Give the extent of all Trypanosoma brucei.
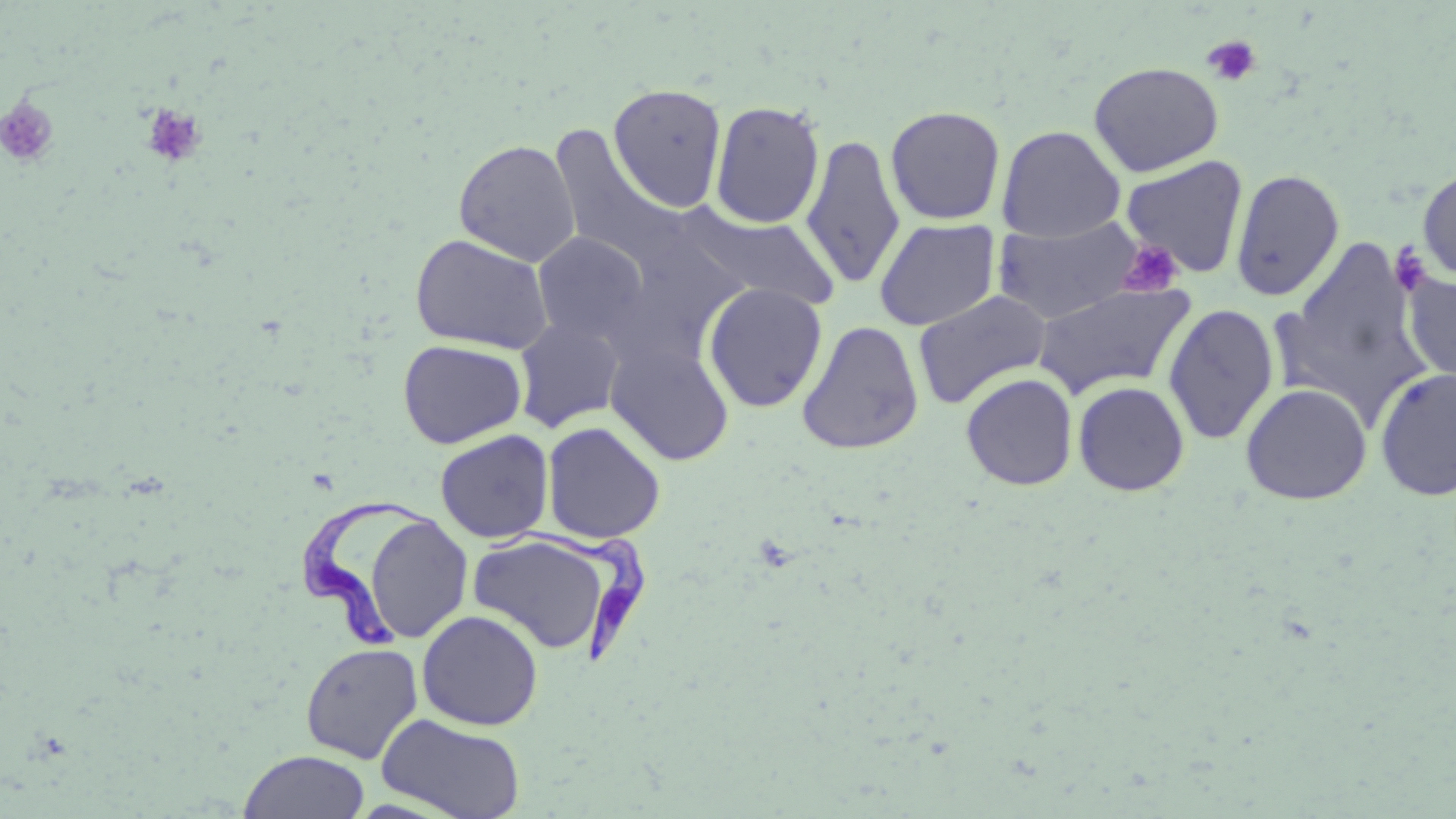

Approximate bounding boxes as named x1/y1/x2/y2 corners in pixels.
Trypanosoma brucei: (x1=299, y1=496, x2=452, y2=650), (x1=484, y1=519, x2=649, y2=666).

slide_level_diagnosis: Trypanosoma brucei
modality: optical microscopy
image_size: 1456×819 pixels
preparation: thin blood smear
field_of_view: single
platelet_locations: 'approximate bounding boxes as named x1/y1/x2/y2 corners in pixels: (x1=1202, y1=36, x2=1261, y2=87), (x1=0, y1=96, x2=60, y2=168), (x1=141, y1=104, x2=208, y2=168), (x1=1116, y1=239, x2=1183, y2=297), (x1=1387, y1=242, x2=1434, y2=298)'
stain: May-Grünwald-Giemsa
uninfected_red_blood_cell_locations: 'approximate bounding boxes as named x1/y1/x2/y2 corners in pixels: (x1=1089, y1=61, x2=1224, y2=176), (x1=608, y1=83, x2=726, y2=212), (x1=710, y1=100, x2=825, y2=230), (x1=885, y1=105, x2=1006, y2=225), (x1=548, y1=125, x2=687, y2=271), (x1=997, y1=125, x2=1125, y2=242), (x1=800, y1=133, x2=905, y2=289), (x1=454, y1=139, x2=580, y2=267), (x1=1120, y1=155, x2=1249, y2=278), (x1=1417, y1=165, x2=1456, y2=282), (x1=1230, y1=168, x2=1345, y2=301), (x1=682, y1=209, x2=842, y2=312), (x1=991, y1=217, x2=1145, y2=324), (x1=873, y1=218, x2=1000, y2=331), (x1=599, y1=230, x2=750, y2=371), (x1=533, y1=232, x2=650, y2=345), (x1=410, y1=233, x2=554, y2=355), (x1=1286, y1=240, x2=1424, y2=395), (x1=1403, y1=272, x2=1456, y2=387), (x1=1030, y1=281, x2=1196, y2=400), (x1=702, y1=283, x2=828, y2=413), (x1=912, y1=289, x2=1052, y2=409), (x1=1162, y1=302, x2=1280, y2=445), (x1=514, y1=317, x2=626, y2=433), (x1=797, y1=320, x2=924, y2=455), (x1=397, y1=339, x2=527, y2=449), (x1=606, y1=341, x2=735, y2=466), (x1=1374, y1=367, x2=1456, y2=502), (x1=961, y1=373, x2=1077, y2=490), (x1=1073, y1=381, x2=1190, y2=497), (x1=1240, y1=383, x2=1372, y2=504), (x1=542, y1=421, x2=665, y2=544), (x1=435, y1=430, x2=554, y2=543), (x1=361, y1=512, x2=472, y2=644), (x1=468, y1=534, x2=612, y2=654), (x1=416, y1=609, x2=544, y2=730), (x1=300, y1=642, x2=423, y2=764), (x1=376, y1=713, x2=526, y2=819), (x1=238, y1=750, x2=370, y2=819)'
magnification: 1000x